Identify the blood parasite species.
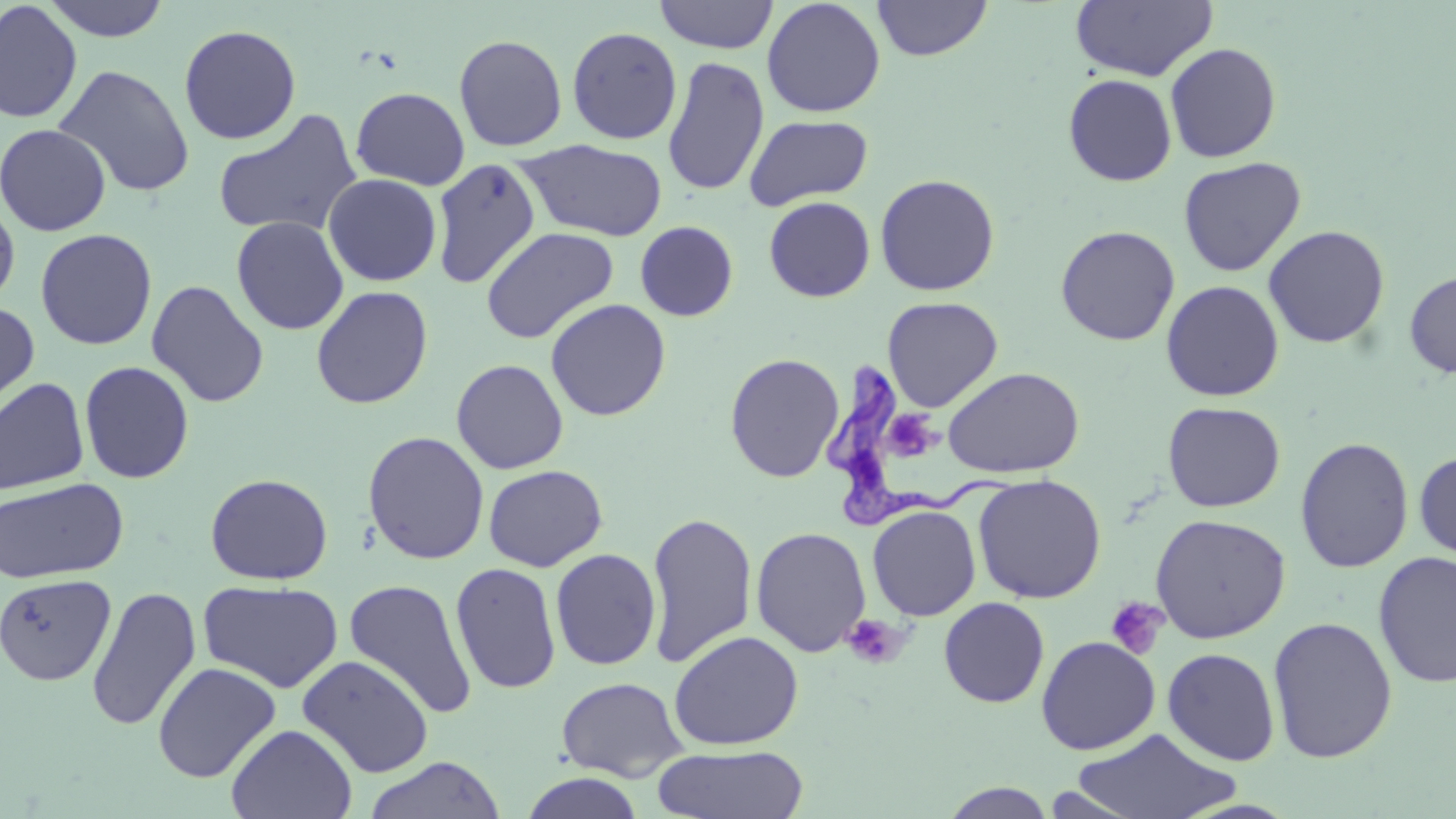

Trypanosoma brucei.

Approximate bounding boxes as named x1/y1/x2/y2 corners in pixels. Trypanosoma brucei locations: (x1=821, y1=353, x2=1015, y2=529). Uninfected red blood cell locations: (x1=41, y1=0, x2=172, y2=41), (x1=654, y1=0, x2=778, y2=54), (x1=761, y1=0, x2=886, y2=118), (x1=872, y1=0, x2=993, y2=61), (x1=1070, y1=0, x2=1218, y2=82), (x1=0, y1=1, x2=82, y2=124), (x1=178, y1=24, x2=301, y2=144), (x1=566, y1=26, x2=682, y2=144), (x1=453, y1=34, x2=568, y2=151), (x1=1164, y1=43, x2=1281, y2=163), (x1=662, y1=55, x2=769, y2=196), (x1=53, y1=64, x2=195, y2=198), (x1=1063, y1=74, x2=1177, y2=186), (x1=351, y1=87, x2=470, y2=190), (x1=213, y1=108, x2=363, y2=238), (x1=743, y1=115, x2=873, y2=210), (x1=0, y1=123, x2=111, y2=236), (x1=518, y1=140, x2=669, y2=241), (x1=1177, y1=156, x2=1306, y2=276), (x1=431, y1=158, x2=541, y2=288), (x1=323, y1=173, x2=442, y2=286), (x1=874, y1=173, x2=1000, y2=296), (x1=0, y1=196, x2=20, y2=311), (x1=763, y1=196, x2=875, y2=302), (x1=231, y1=216, x2=349, y2=335), (x1=635, y1=220, x2=738, y2=321), (x1=1263, y1=224, x2=1390, y2=349), (x1=1055, y1=225, x2=1180, y2=346), (x1=481, y1=226, x2=619, y2=344), (x1=35, y1=228, x2=157, y2=350), (x1=1403, y1=268, x2=1456, y2=379), (x1=146, y1=279, x2=269, y2=408), (x1=1160, y1=280, x2=1284, y2=401), (x1=311, y1=286, x2=433, y2=409), (x1=882, y1=296, x2=1003, y2=412), (x1=545, y1=298, x2=671, y2=421), (x1=0, y1=301, x2=40, y2=423), (x1=724, y1=352, x2=845, y2=483), (x1=450, y1=358, x2=569, y2=474), (x1=79, y1=361, x2=195, y2=483), (x1=943, y1=366, x2=1084, y2=478), (x1=0, y1=377, x2=90, y2=495), (x1=1162, y1=401, x2=1286, y2=512), (x1=362, y1=431, x2=489, y2=565), (x1=1294, y1=436, x2=1415, y2=573), (x1=1414, y1=450, x2=1456, y2=564), (x1=483, y1=465, x2=608, y2=571), (x1=205, y1=473, x2=333, y2=585), (x1=972, y1=474, x2=1106, y2=604), (x1=0, y1=477, x2=128, y2=584), (x1=867, y1=505, x2=981, y2=620), (x1=645, y1=510, x2=758, y2=670), (x1=1149, y1=513, x2=1291, y2=643), (x1=751, y1=526, x2=871, y2=656), (x1=550, y1=548, x2=661, y2=670), (x1=1373, y1=551, x2=1456, y2=689), (x1=450, y1=561, x2=562, y2=694), (x1=0, y1=573, x2=117, y2=686), (x1=343, y1=577, x2=478, y2=721), (x1=197, y1=580, x2=344, y2=693), (x1=86, y1=586, x2=201, y2=732), (x1=939, y1=597, x2=1050, y2=707), (x1=1267, y1=615, x2=1398, y2=764), (x1=669, y1=630, x2=804, y2=750), (x1=1035, y1=636, x2=1161, y2=755), (x1=1162, y1=647, x2=1281, y2=766), (x1=297, y1=654, x2=435, y2=778), (x1=152, y1=661, x2=281, y2=783), (x1=556, y1=676, x2=687, y2=781), (x1=225, y1=724, x2=358, y2=819), (x1=1070, y1=728, x2=1240, y2=818), (x1=651, y1=744, x2=809, y2=819), (x1=364, y1=756, x2=506, y2=819), (x1=520, y1=773, x2=646, y2=819), (x1=939, y1=782, x2=1057, y2=819). Platelet locations: (x1=885, y1=404, x2=941, y2=462), (x1=1106, y1=597, x2=1169, y2=659), (x1=841, y1=614, x2=906, y2=669). May-Grünwald-Giemsa stain. Single field of view. Optical microscopy. Thin blood film. 1000x magnification. Image is 1456×819 pixels.